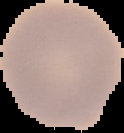
Summary:
  - Result: no malaria parasites seen
  - Preparation: thin blood film
  - Image size: 124×133 pixels
  - Image type: segmented cell region with the area outside set to black